Locate every leukocyte (white blood cell).
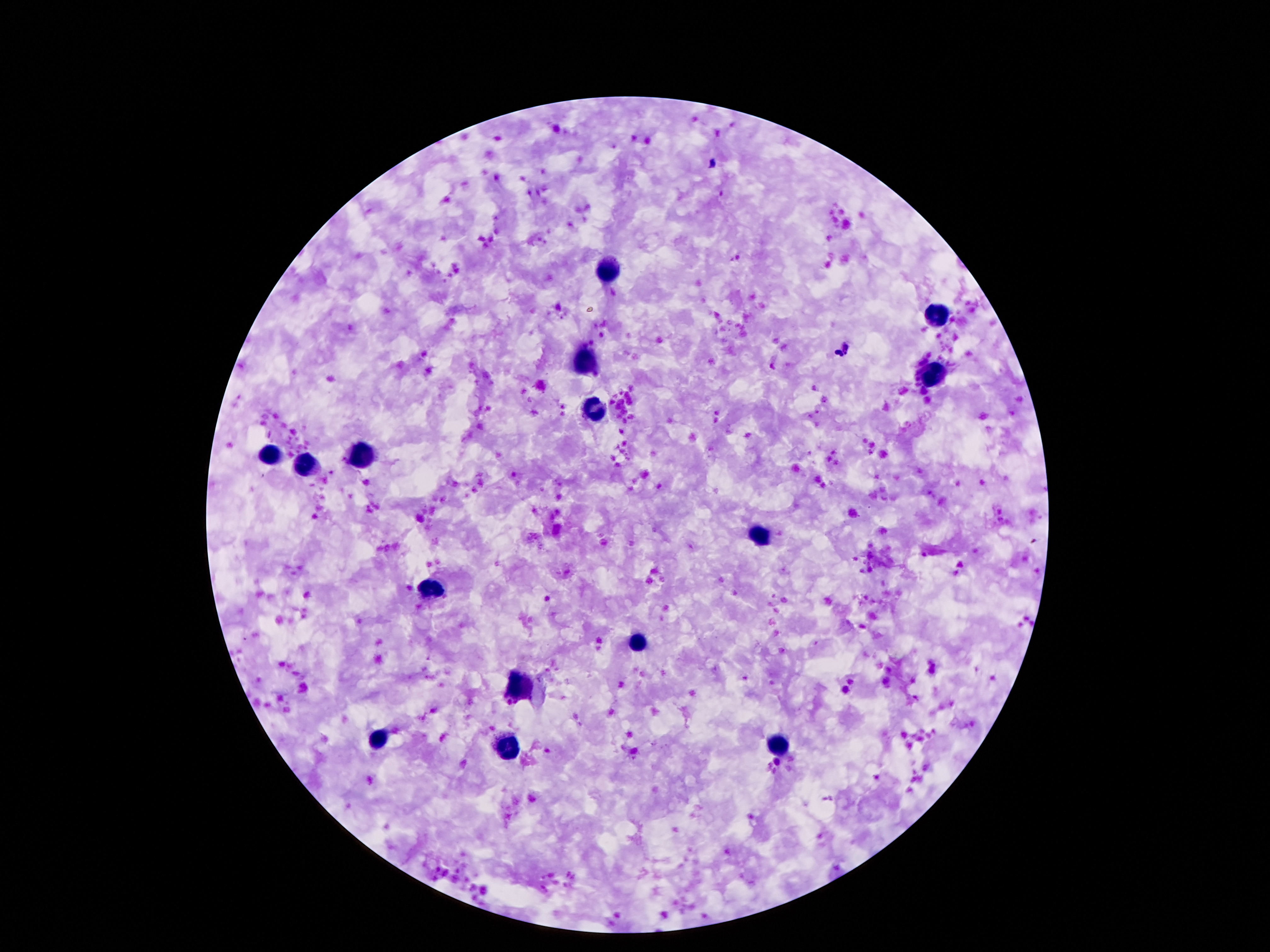
Approximate centers as (x, y) in pixels.
Leukocytes: (608, 269), (932, 315), (585, 362), (930, 374), (597, 409), (270, 457), (363, 457), (307, 465), (760, 535), (436, 589), (639, 643), (520, 685), (380, 739), (776, 746), (508, 748).

{
  "preparation": "thick blood film",
  "magnification": "100x",
  "image_size": "1270×952 pixels",
  "field_of_view": "one from this slide",
  "capture": "smartphone camera through the microscope eyepiece",
  "stain": "Giemsa",
  "patient_malaria_status": "negative"
}